State the blood parasite species.
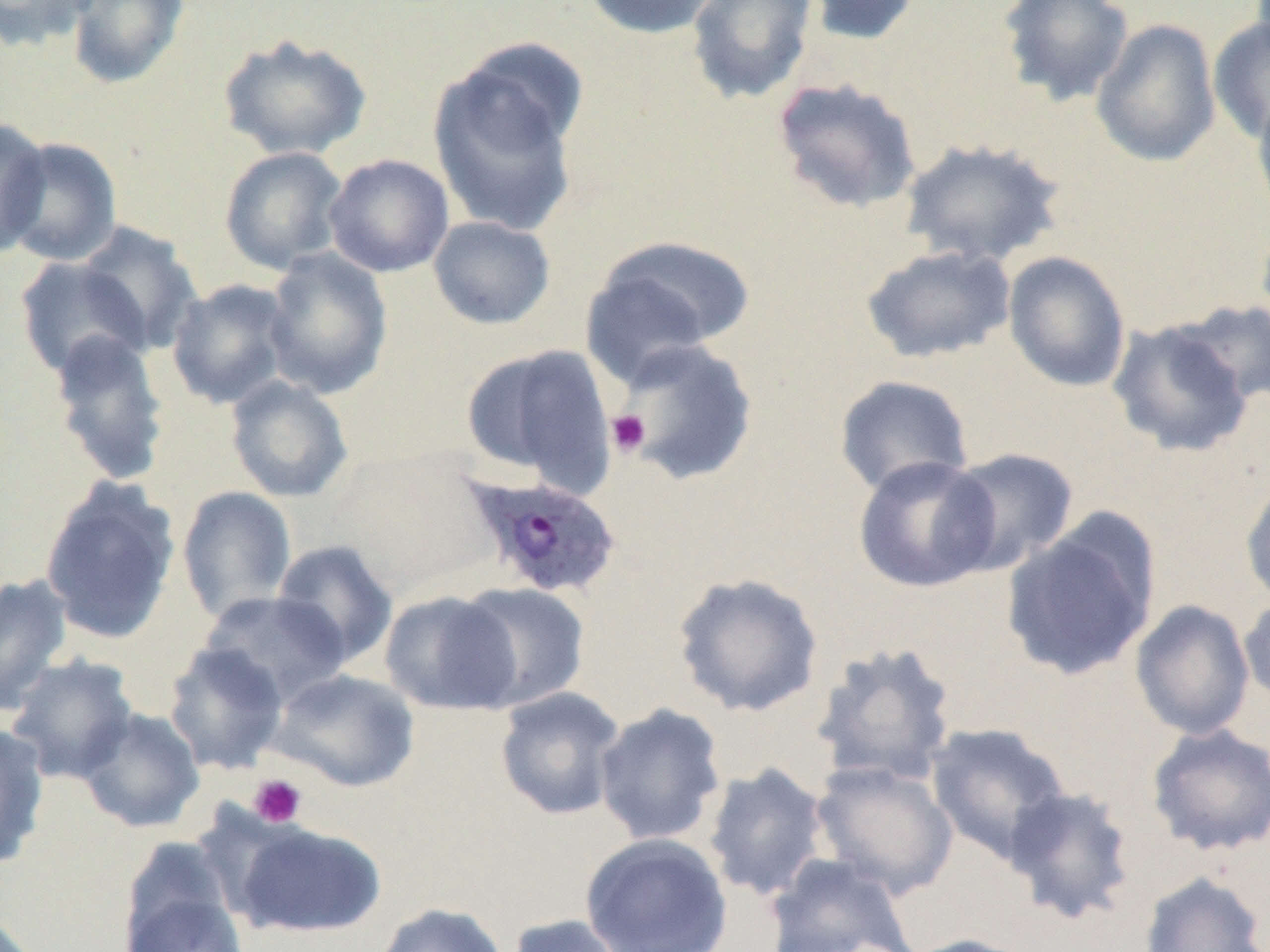

Plasmodium ovale.

Summary:
  - Coordinate format: approximate bounding boxes as (x1, y1, x2, y2) in pixels
  - Platelet locations: (606, 410, 650, 457), (248, 774, 307, 828)
  - Uninfected red blood cell locations: (0, 0, 96, 51), (65, 0, 190, 90), (581, 0, 722, 40), (685, 0, 819, 106), (803, 0, 924, 46), (996, 0, 1135, 107), (1208, 16, 1270, 144), (1090, 18, 1221, 168), (218, 33, 373, 161), (427, 48, 586, 238), (770, 76, 923, 216), (1252, 88, 1270, 224), (0, 116, 52, 258), (2, 136, 123, 267), (898, 138, 1067, 269), (219, 145, 349, 276), (323, 154, 454, 278), (1255, 213, 1270, 342), (427, 215, 556, 330), (75, 221, 205, 354), (581, 235, 756, 381), (860, 244, 1017, 364), (262, 247, 393, 400), (1002, 251, 1131, 393), (14, 256, 151, 380), (166, 279, 296, 410), (1178, 298, 1270, 408), (1106, 319, 1253, 458), (47, 330, 172, 486), (613, 337, 759, 487), (460, 342, 617, 493), (225, 375, 354, 503), (833, 375, 975, 498), (330, 446, 496, 595), (942, 447, 1081, 575), (852, 455, 1001, 593), (1239, 475, 1270, 609), (39, 478, 181, 645), (176, 486, 297, 623), (1000, 517, 1159, 681), (271, 540, 399, 668), (671, 571, 826, 718), (0, 573, 74, 714), (455, 582, 591, 711), (379, 589, 523, 715), (198, 590, 350, 709), (1238, 593, 1270, 710), (1130, 600, 1255, 740), (163, 641, 289, 775), (811, 641, 959, 788), (4, 653, 140, 784), (269, 669, 420, 793), (494, 687, 627, 821), (593, 702, 727, 846), (76, 707, 205, 833), (0, 722, 51, 870), (925, 722, 1072, 864), (1145, 723, 1270, 857), (809, 759, 959, 901), (702, 762, 830, 903), (1002, 785, 1138, 925), (233, 821, 386, 938), (581, 832, 733, 952), (762, 853, 919, 952), (1137, 870, 1269, 951), (121, 881, 249, 952), (374, 902, 510, 952), (504, 914, 633, 952), (897, 933, 1037, 952)
  - Plasmodium ovale-infected red blood cell locations: (463, 474, 622, 600)
  - Preparation: thin blood smear
  - Modality: optical microscopy
  - Field of view: one of a larger specimen
  - Magnification: 1000x
  - Image size: 1270×952 pixels